Assess the morphology of the erythrocytes.
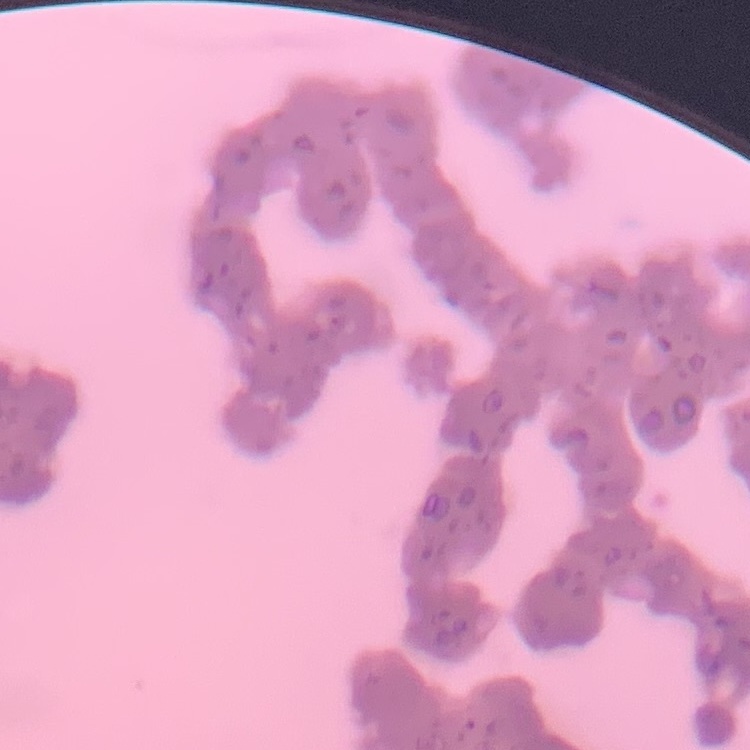
They show rouleaux formation.

Summary:
  - Preparation: thin blood smear
  - Stain: Field's or Giemsa
  - Image type: one tile cut from a larger photomicrograph